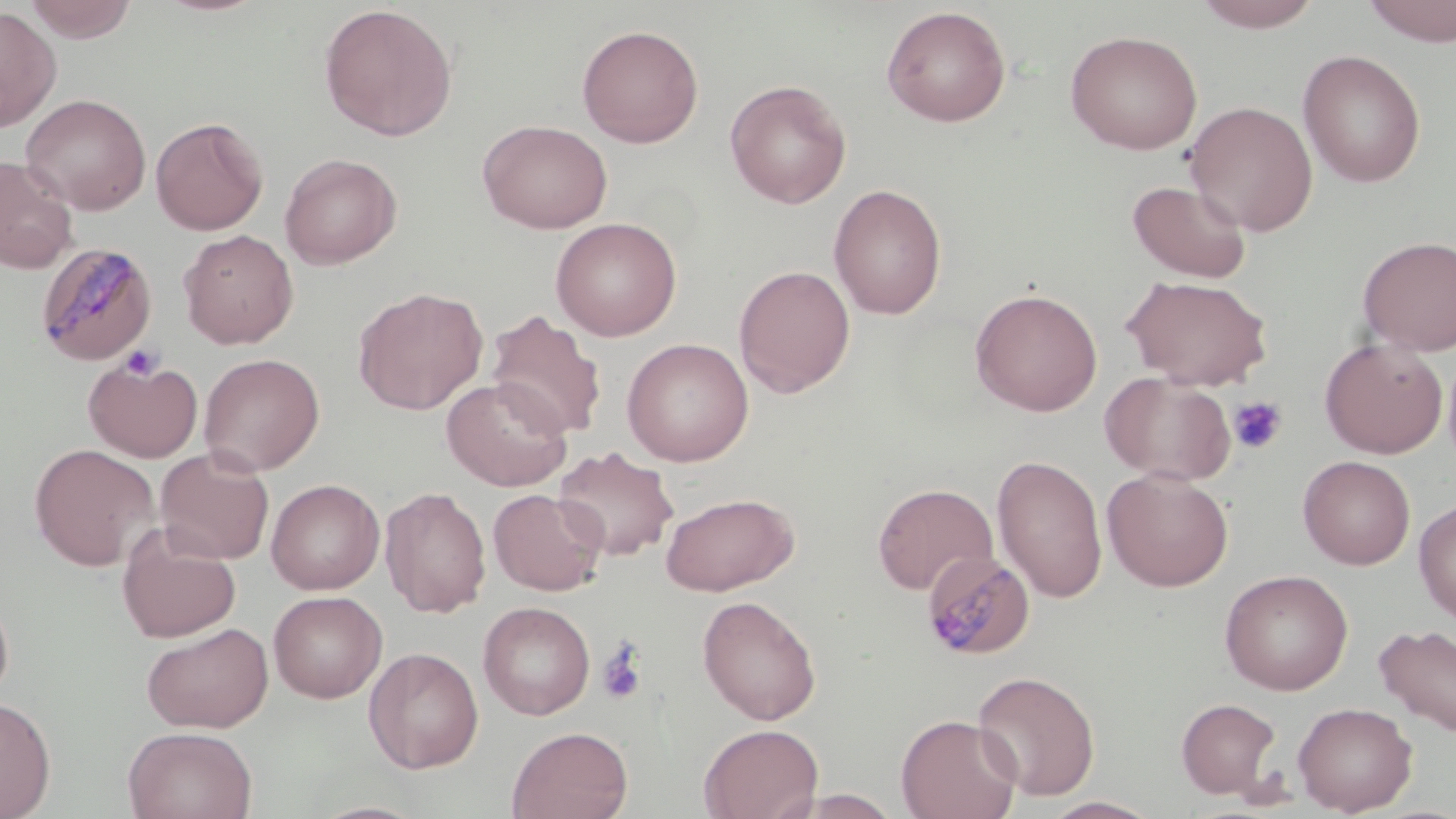 Approximate bounding boxes as [x1, y1, x2, y2] in pixels. Platelet locations: [118, 344, 165, 382], [1227, 396, 1288, 455], [596, 643, 646, 706]. Uninfected red blood cell locations: [24, 0, 137, 43], [1191, 0, 1325, 32], [1360, 1, 1456, 46], [318, 4, 457, 142], [881, 5, 1011, 126], [0, 6, 61, 132], [576, 24, 704, 148], [1065, 29, 1203, 155], [1297, 49, 1426, 188], [725, 79, 851, 209], [21, 93, 151, 215], [1184, 100, 1318, 236], [150, 116, 268, 235], [477, 119, 613, 234], [279, 152, 401, 269], [0, 154, 78, 274], [1126, 179, 1252, 284], [828, 183, 947, 320], [549, 217, 682, 341], [178, 229, 299, 349], [1358, 235, 1456, 355], [734, 264, 856, 398], [1121, 275, 1273, 390], [352, 287, 488, 415], [970, 287, 1103, 416], [486, 310, 607, 441], [621, 337, 754, 467], [1319, 337, 1448, 458], [199, 352, 325, 476], [83, 354, 203, 463], [1101, 371, 1237, 486], [441, 376, 573, 491], [29, 443, 159, 571], [155, 446, 275, 564], [553, 446, 679, 561], [991, 454, 1108, 604], [1298, 455, 1415, 569], [1102, 468, 1234, 592], [266, 478, 385, 594], [872, 482, 998, 595], [380, 486, 492, 618], [488, 488, 606, 596], [659, 492, 799, 595], [1414, 498, 1456, 626], [117, 523, 240, 642], [1219, 569, 1353, 695], [0, 589, 14, 705], [268, 590, 387, 702], [697, 595, 821, 725], [478, 601, 595, 719], [142, 622, 273, 733], [1374, 624, 1456, 738], [363, 646, 484, 774], [972, 670, 1100, 801], [0, 695, 56, 819], [1176, 698, 1281, 799], [1292, 702, 1418, 816], [895, 713, 1022, 819], [698, 723, 823, 819], [507, 725, 633, 819], [123, 726, 257, 819], [783, 789, 906, 819], [1039, 796, 1164, 818]. Plasmodium malariae-infected red blood cell locations: [35, 241, 158, 366], [923, 554, 1039, 663]. Slide-level diagnosis: Plasmodium malariae. Image is 1456×819 pixels. Optical microscopy. Single field of view. Thin blood film. Captured at 1000x magnification. May-Grünwald-Giemsa-stained preparation.